Identify the blood parasite species.
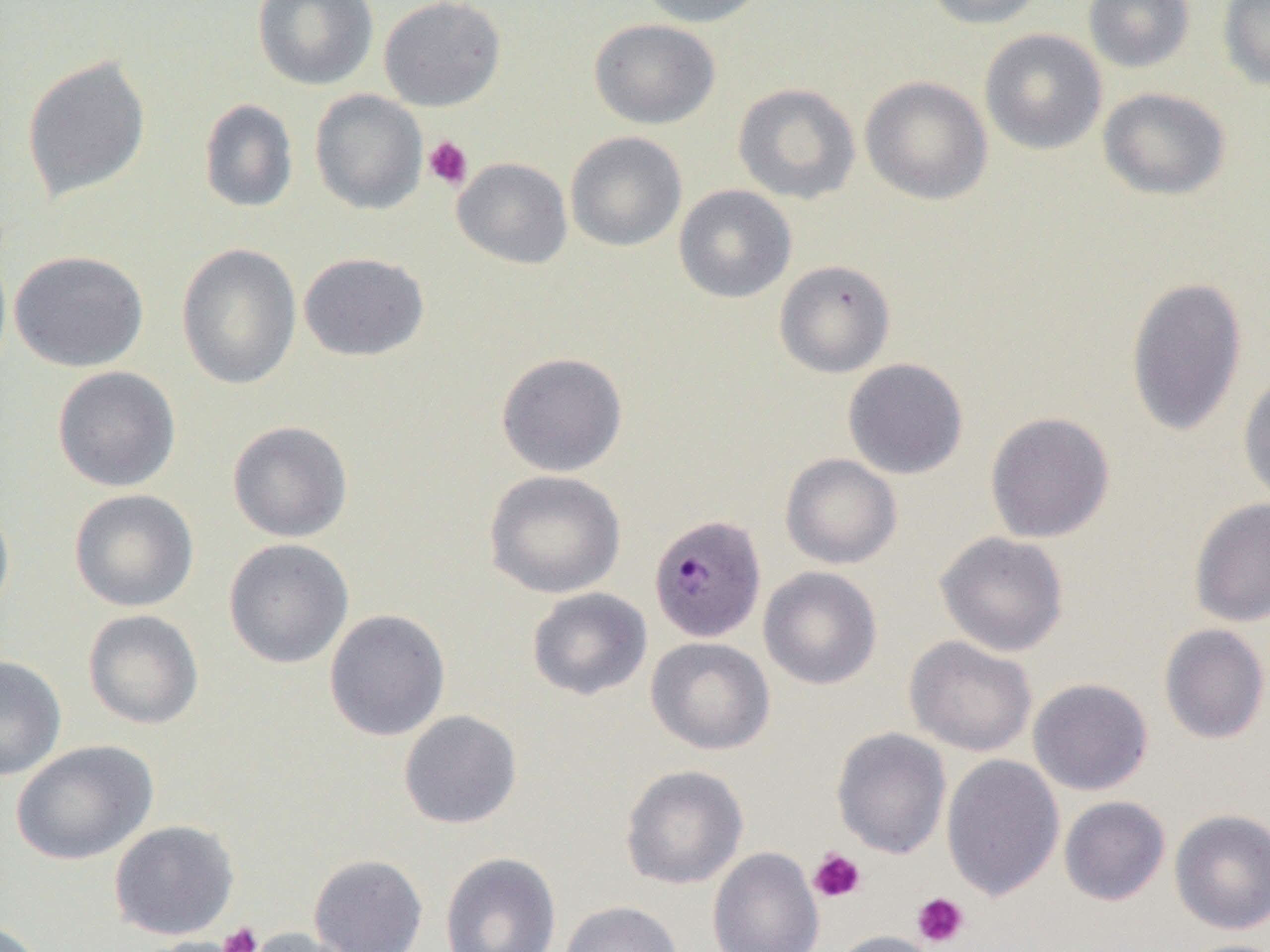

Plasmodium malariae.

Approximate bounding boxes as (x1, y1, x2, y2) in pixels. Plasmodium malariae-infected red blood cell locations: (649, 513, 767, 643). Uninfected red blood cell locations: (252, 0, 378, 91), (379, 0, 506, 112), (637, 0, 769, 27), (924, 0, 1047, 29), (1083, 0, 1195, 72), (1218, 0, 1270, 92), (589, 19, 721, 129), (979, 28, 1107, 154), (21, 54, 152, 203), (860, 75, 993, 205), (733, 83, 861, 205), (1098, 87, 1231, 201), (309, 89, 428, 215), (198, 98, 299, 213), (565, 131, 687, 252), (452, 157, 572, 269), (674, 184, 796, 303), (176, 242, 302, 391), (9, 250, 149, 373), (298, 252, 430, 362), (774, 260, 896, 378), (1125, 276, 1248, 437), (496, 352, 628, 477), (842, 357, 968, 480), (52, 366, 181, 492), (1237, 371, 1270, 506), (985, 411, 1116, 543), (227, 421, 353, 542), (779, 453, 902, 569), (484, 469, 627, 599), (68, 489, 199, 612), (1189, 497, 1270, 627), (0, 500, 15, 627), (934, 531, 1070, 657), (223, 538, 354, 669), (758, 566, 883, 690), (527, 587, 652, 701), (83, 609, 204, 730), (324, 609, 450, 742), (1158, 623, 1270, 744), (904, 635, 1037, 757), (646, 637, 775, 755), (0, 654, 67, 780), (1028, 678, 1154, 795), (398, 710, 522, 829), (831, 727, 952, 859), (11, 740, 157, 866), (941, 754, 1064, 902), (620, 764, 749, 889), (1059, 796, 1171, 906), (1169, 808, 1270, 935), (109, 820, 240, 940), (707, 847, 824, 952), (440, 852, 562, 952), (308, 854, 428, 952), (558, 900, 684, 952), (0, 917, 48, 952), (241, 926, 364, 952), (830, 930, 943, 952), (138, 936, 255, 952), (1176, 938, 1270, 952). Platelet locations: (422, 135, 474, 190), (808, 848, 867, 903), (912, 892, 969, 948), (219, 922, 263, 952). Optical microscopy. 1000x magnification. Thin blood smear. One field of a larger specimen. Image is 1270×952 pixels.